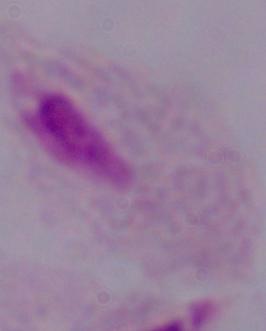
Summary:
  - Magnification: 1000x
  - Modality: micrograph
  - Identification: trichomonad